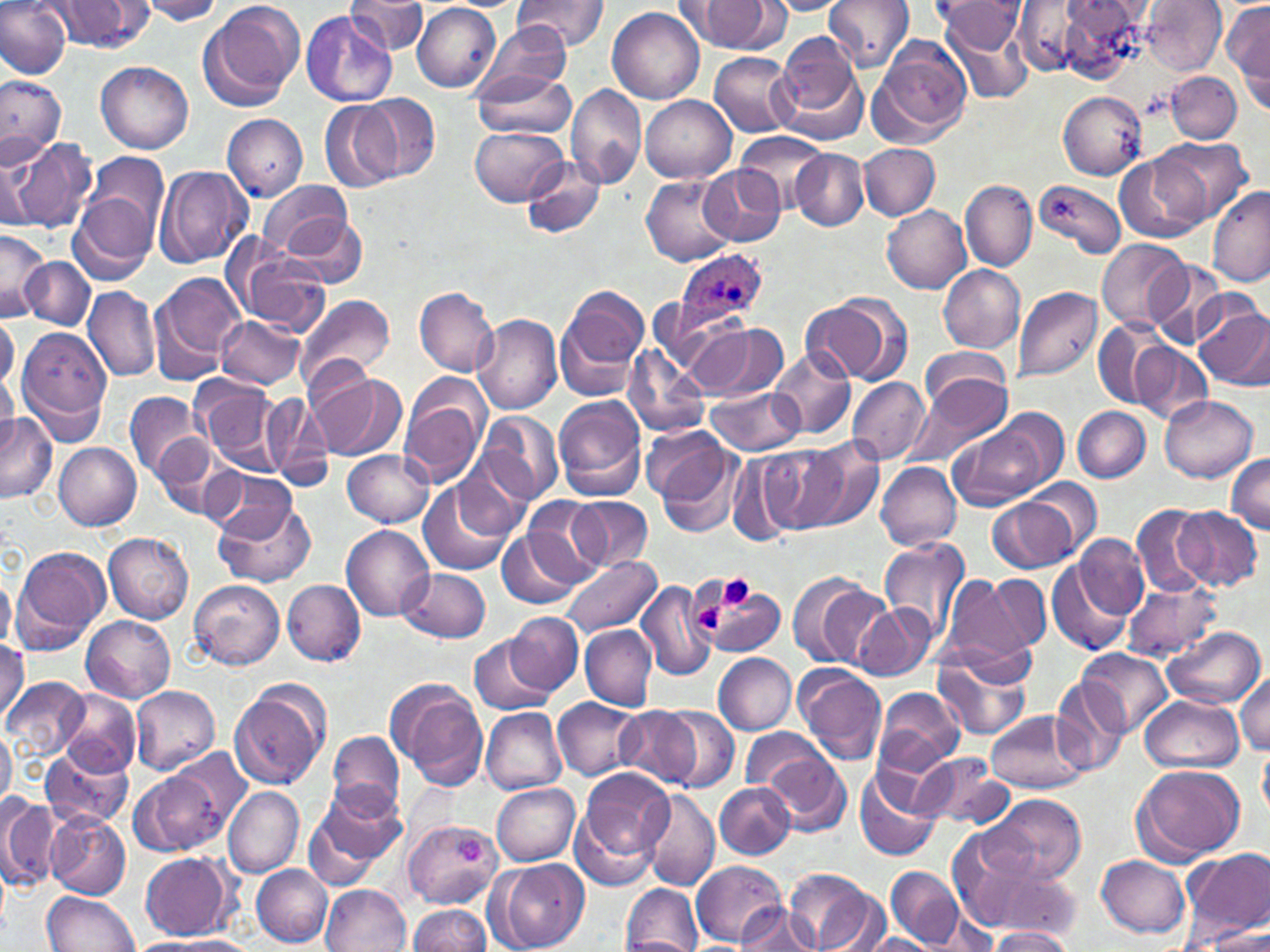

slide-level diagnosis = Plasmodium ovale
magnification = 1000x
stain = May-Grünwald-Giemsa
uninfected red blood cell locations = approximate bounding boxes as (x1,y1)-(x2,y2) corner pairs in pixels: (0,0)-(72,80), (135,0)-(228,24), (199,0)-(306,110), (345,0)-(428,57), (512,0)-(609,53), (822,0)-(914,70), (1142,0)-(1226,73), (44,1)-(156,53), (765,1)-(848,16), (938,2)-(1025,53), (1011,2)-(1096,75), (1045,2)-(1148,81), (1223,2)-(1269,101), (686,3)-(772,51), (412,4)-(501,92), (607,5)-(705,103), (301,9)-(398,107), (942,18)-(1035,106), (475,22)-(574,103), (773,34)-(866,141), (872,36)-(973,142), (709,52)-(798,137), (97,61)-(194,154), (470,69)-(576,139), (1165,71)-(1241,143), (0,74)-(64,161), (566,82)-(650,191), (1057,91)-(1147,178), (359,95)-(440,182), (640,95)-(735,182), (319,100)-(400,193), (221,114)-(309,200), (471,126)-(568,207), (736,132)-(829,212), (1153,137)-(1249,227), (10,138)-(98,234), (860,143)-(940,220), (791,149)-(869,229), (88,152)-(170,237), (1114,154)-(1208,244), (0,155)-(43,237), (519,157)-(605,239), (697,164)-(784,246), (156,166)-(250,269), (641,176)-(734,266), (959,179)-(1036,272), (1035,179)-(1126,258), (258,181)-(354,259), (1208,187)-(1270,287), (67,188)-(162,286), (882,205)-(972,293), (278,210)-(370,289), (0,229)-(48,320), (227,238)-(331,334), (1095,241)-(1187,332), (22,256)-(97,330), (1146,260)-(1230,349), (939,265)-(1023,352), (149,272)-(245,380), (558,283)-(648,395), (82,286)-(161,382), (1013,286)-(1102,383), (414,287)-(498,376), (296,293)-(395,392), (802,294)-(909,386), (1194,299)-(1270,392), (658,309)-(748,391), (0,313)-(19,394), (471,314)-(561,415), (216,315)-(303,388), (1091,320)-(1168,410), (688,321)-(787,401), (16,328)-(114,442), (1131,341)-(1212,425), (621,345)-(709,438), (771,347)-(855,440), (919,348)-(1012,424), (0,357)-(19,445), (312,373)-(405,461), (910,374)-(1013,468), (194,376)-(285,475), (845,376)-(929,466), (399,378)-(489,489), (707,385)-(804,455), (123,391)-(206,483), (261,391)-(334,489), (1160,395)-(1257,482), (553,397)-(646,501), (1073,406)-(1148,482), (476,409)-(564,505), (0,412)-(56,502), (949,413)-(1061,510), (641,426)-(730,503), (155,438)-(238,522), (652,438)-(746,539), (797,439)-(883,534), (54,443)-(142,530), (760,444)-(849,533), (343,448)-(433,527), (729,456)-(800,546), (1228,456)-(1270,533), (877,462)-(962,552), (204,469)-(301,545), (1024,478)-(1103,556), (418,480)-(515,577), (989,494)-(1082,573), (566,496)-(653,572), (520,497)-(610,587), (214,498)-(316,588), (1131,502)-(1212,598), (1173,505)-(1262,591), (342,525)-(434,621), (499,529)-(587,609), (104,532)-(193,624), (1074,534)-(1148,623), (881,537)-(970,644), (10,547)-(111,654), (561,557)-(659,637), (1047,557)-(1133,658), (400,568)-(491,643), (789,572)-(887,669), (0,574)-(16,651), (939,574)-(1039,676), (984,576)-(1051,654), (187,578)-(284,672), (636,579)-(716,683), (283,580)-(365,666), (1121,580)-(1220,661), (700,588)-(786,654), (852,602)-(934,682), (509,611)-(584,696), (82,616)-(175,703), (580,625)-(657,711), (1161,626)-(1265,710), (468,633)-(556,715), (0,639)-(27,721), (931,645)-(1034,741), (1078,649)-(1173,737), (713,652)-(797,734), (795,665)-(887,765), (1233,671)-(1270,757), (1,676)-(89,763), (388,679)-(488,790), (1051,680)-(1132,776), (229,681)-(331,791), (130,687)-(220,774), (876,688)-(964,775), (58,689)-(141,778), (1141,695)-(1242,773), (554,696)-(643,780), (656,706)-(738,792), (614,707)-(702,789), (480,708)-(568,796), (985,709)-(1088,792), (741,727)-(834,795), (0,729)-(16,809), (328,729)-(404,817), (41,746)-(131,829), (1258,747)-(1270,820), (760,749)-(850,836), (911,752)-(1012,831), (129,764)-(234,859), (1132,764)-(1245,865), (578,767)-(674,870), (856,769)-(942,864), (490,782)-(580,865), (715,783)-(795,859), (305,784)-(406,885), (223,786)-(304,877), (641,790)-(719,891), (985,792)-(1086,884), (0,794)-(61,892), (571,810)-(657,891), (45,812)-(130,899), (404,817)-(500,912), (947,828)-(1060,933), (1182,848)-(1269,943), (139,852)-(236,940), (1096,854)-(1191,937), (691,858)-(788,946), (491,859)-(589,952), (251,864)-(332,947), (885,866)-(964,948), (786,868)-(878,951), (995,869)-(1081,941), (620,884)-(702,951), (321,885)-(410,952), (41,891)-(137,951), (732,903)-(819,951), (407,904)-(493,952), (996,904)-(1074,946), (924,912)-(1000,952), (1199,922)-(1270,949), (989,927)-(1073,951), (855,933)-(941,951), (142,935)-(261,952)
preparation = thin blood film
Plasmodium ovale-infected red blood cell locations = approximate bounding boxes as (x1,y1)-(x2,y2) corner pairs in pixels: (675,249)-(767,330)
modality = light microscopy
image size = 1270×952 pixels
platelet locations = approximate bounding boxes as (x1,y1)-(x2,y2) corner pairs in pixels: (717,575)-(755,611), (692,599)-(725,636)
field of view = single